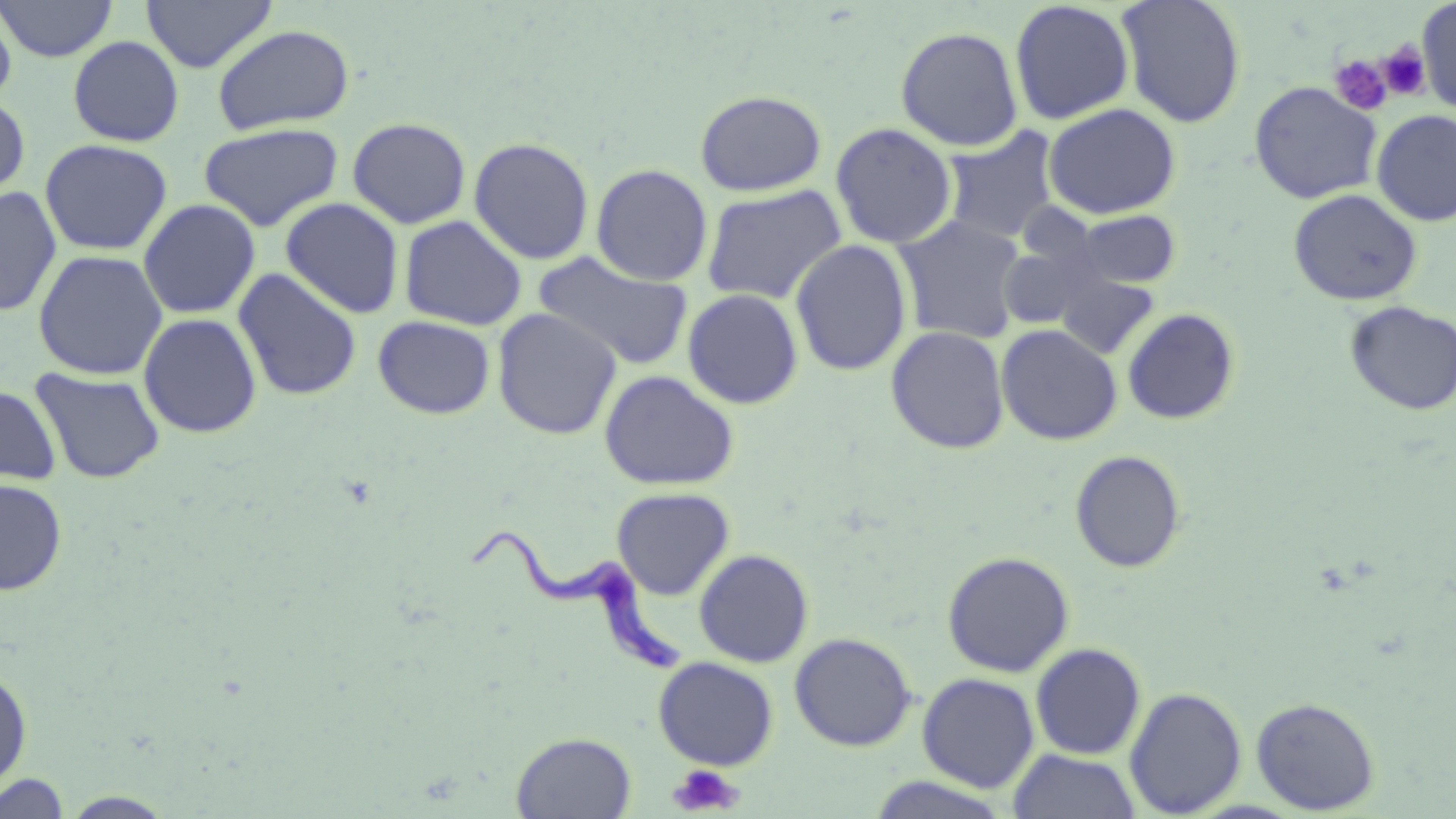
slide_level_diagnosis: Trypanosoma brucei
preparation: thin blood film
magnification: 1000x
field_of_view: one of a larger specimen
trypanosoma_brucei_locations: 'approximate bounding boxes as (x1,y1)-(x2,y2) corner pairs in pixels: (466,521)-(689,676)'
stain: May-Grünwald-Giemsa
uninfected_red_blood_cell_locations: 'approximate bounding boxes as (x1,y1)-(x2,y2) corner pairs in pixels: (2,0)-(118,62), (141,0)-(277,73), (1116,0)-(1247,128), (1008,1)-(1135,125), (1416,2)-(1456,115), (0,3)-(17,109), (212,23)-(356,135), (895,25)-(1024,151), (67,35)-(184,147), (1248,80)-(1382,204), (695,89)-(827,196), (0,94)-(31,202), (1043,103)-(1181,219), (1371,109)-(1456,226), (347,117)-(471,228), (198,122)-(343,232), (830,122)-(958,249), (940,127)-(1061,244), (468,136)-(595,265), (39,138)-(172,255), (590,163)-(713,286), (700,183)-(848,304), (0,186)-(61,316), (1288,188)-(1422,306), (280,197)-(404,319), (138,198)-(260,319), (1066,209)-(1182,290), (399,215)-(527,331), (893,215)-(1027,344), (790,239)-(912,376), (998,241)-(1102,331), (32,249)-(168,380), (533,252)-(694,370), (233,267)-(362,401), (1055,273)-(1159,359), (682,288)-(803,409), (1344,301)-(1456,415), (492,307)-(622,440), (1121,307)-(1241,425), (138,312)-(261,439), (372,315)-(495,419), (996,323)-(1122,445), (886,325)-(1009,454), (30,367)-(166,484), (599,370)-(739,490), (0,383)-(61,486), (1069,450)-(1187,573), (0,478)-(67,595), (611,487)-(735,600), (694,548)-(814,667), (942,551)-(1075,677), (789,632)-(917,751), (1030,643)-(1146,760), (653,656)-(779,770), (0,665)-(33,795), (917,672)-(1040,792), (1124,686)-(1247,817), (1251,696)-(1380,814), (511,731)-(637,818), (1008,749)-(1141,819), (0,772)-(72,818)'
image_size: 1456×819 pixels
modality: optical microscopy
platelet_locations: 'approximate bounding boxes as (x1,y1)-(x2,y2) corner pairs in pixels: (1378,42)-(1431,101), (1329,54)-(1393,116), (667,764)-(743,816)'